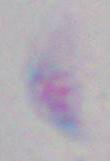

{
  "modality": "micrograph",
  "magnification": "1000x",
  "identification": "Toxoplasma gondii"
}